Assess the morphology of the red blood cells.
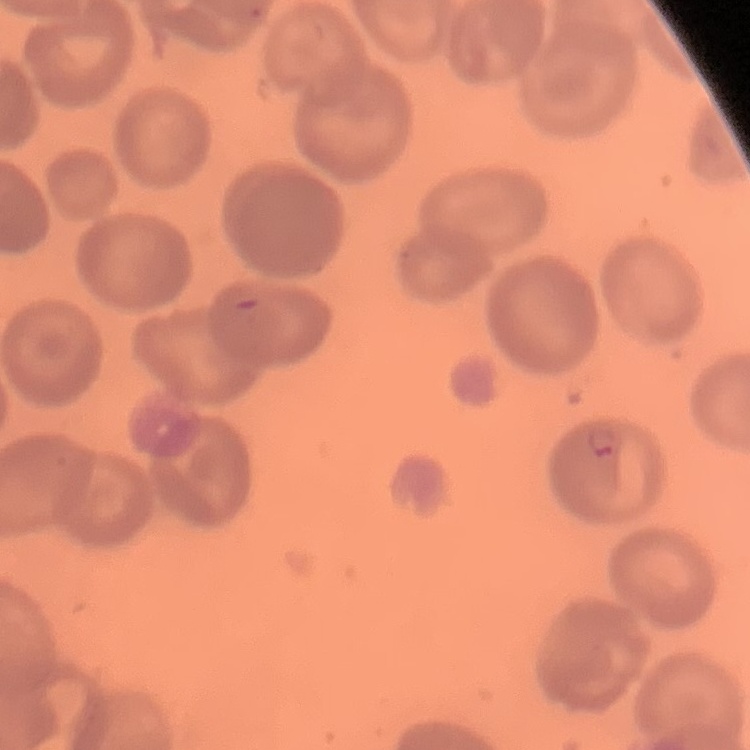

No rouleaux formation.

One tile cut from a larger photomicrograph. Stained with either Field's or Giemsa. Thin blood film.